Locate every blood parasite and identify its species.
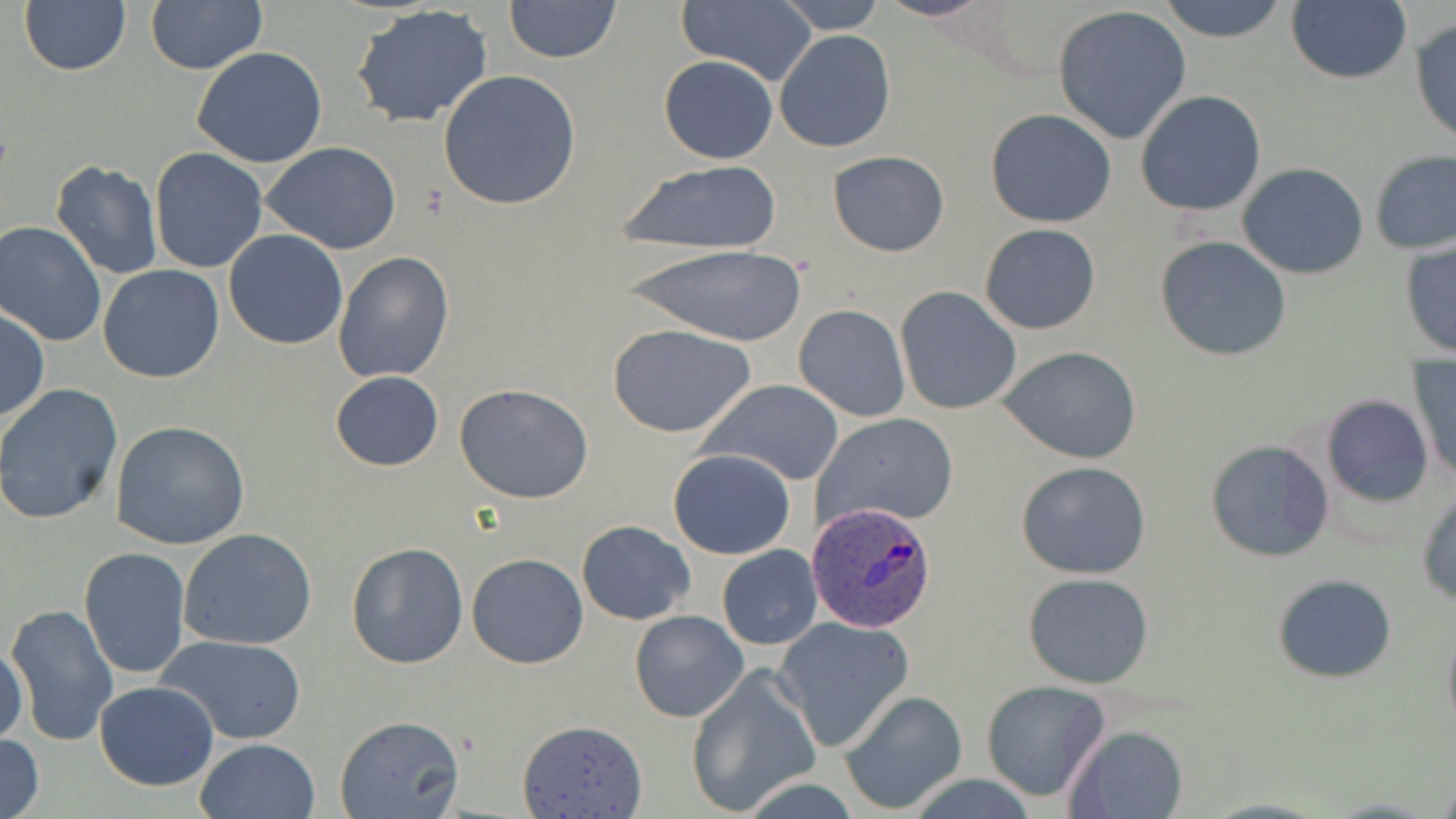

Approximate bounding boxes as (x1, y1, x2, y2) in pixels.
Plasmodium ovale-infected red blood cells: (808, 501, 938, 631).
No Plasmodium falciparum, Plasmodium malariae, Plasmodium vivax, Babesia divergens, or Trypanosoma brucei observed.

Uninfected red blood cell locations: (503, 0, 621, 64), (776, 0, 889, 32), (875, 0, 996, 22), (1156, 0, 1289, 44), (1286, 0, 1411, 86), (19, 1, 131, 76), (146, 2, 266, 74), (675, 3, 818, 84), (349, 5, 495, 129), (1052, 6, 1192, 144), (1409, 15, 1456, 149), (773, 29, 895, 153), (191, 46, 329, 169), (658, 54, 778, 164), (438, 70, 582, 210), (1135, 89, 1268, 217), (984, 109, 1117, 228), (261, 142, 404, 254), (150, 148, 268, 274), (1370, 148, 1456, 256), (828, 151, 950, 256), (49, 159, 163, 281), (613, 159, 785, 257), (1237, 162, 1369, 280), (0, 221, 107, 347), (978, 223, 1101, 334), (223, 229, 347, 350), (1155, 235, 1292, 361), (1399, 239, 1456, 361), (625, 243, 808, 348), (333, 251, 454, 382), (928, 254, 1059, 395), (97, 265, 225, 384), (896, 287, 1022, 413), (794, 304, 910, 423), (0, 306, 48, 425), (609, 324, 757, 438), (1001, 347, 1143, 464), (1410, 358, 1455, 484), (330, 371, 444, 471), (700, 379, 845, 485), (0, 382, 125, 524), (454, 383, 594, 504), (1322, 394, 1434, 507), (813, 414, 960, 529), (110, 419, 252, 552), (1204, 438, 1334, 563), (668, 447, 796, 560), (1015, 461, 1153, 580), (1417, 486, 1456, 608), (577, 520, 695, 626), (178, 528, 318, 650), (345, 542, 469, 667), (717, 545, 822, 650), (78, 547, 192, 681), (467, 553, 588, 670), (1023, 571, 1155, 690), (1271, 573, 1398, 684), (6, 603, 119, 744), (629, 610, 749, 724), (775, 616, 914, 748), (1442, 627, 1456, 737), (159, 635, 306, 744), (0, 643, 29, 749), (686, 665, 823, 816), (980, 680, 1110, 802), (94, 681, 219, 789), (839, 689, 969, 812), (333, 715, 466, 819), (516, 719, 648, 819), (1060, 723, 1190, 819), (0, 733, 46, 819), (194, 737, 322, 819), (907, 774, 1038, 818), (1320, 797, 1439, 817). Slide-level diagnosis: Plasmodium ovale. May-Grünwald-Giemsa stain. Captured at 1000x magnification. Single field of view. Optical microscopy. Thin blood smear. Image is 1456×819 pixels.